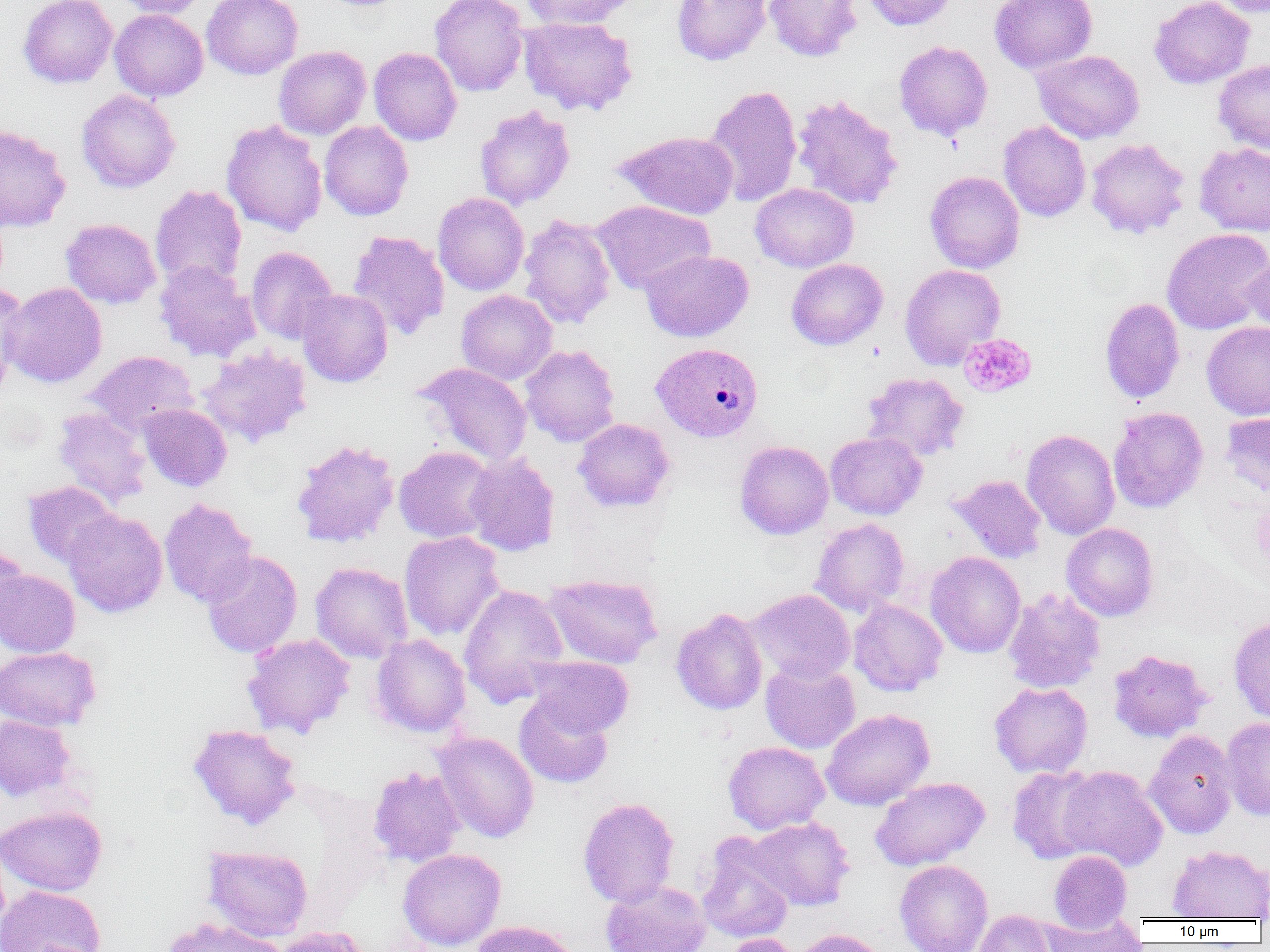

slide-level diagnosis = Plasmodium vivax
uninfected red blood cell locations = approximate bounding boxes as named x1/y1/x2/y2 corners in pixels: (x1=18, y1=0, x2=117, y2=88), (x1=113, y1=0, x2=209, y2=18), (x1=202, y1=0, x2=303, y2=79), (x1=429, y1=0, x2=529, y2=97), (x1=520, y1=0, x2=639, y2=29), (x1=671, y1=0, x2=771, y2=66), (x1=763, y1=0, x2=863, y2=61), (x1=862, y1=0, x2=957, y2=31), (x1=990, y1=0, x2=1098, y2=74), (x1=1149, y1=0, x2=1254, y2=89), (x1=1212, y1=0, x2=1270, y2=18), (x1=109, y1=9, x2=209, y2=101), (x1=518, y1=15, x2=638, y2=116), (x1=894, y1=40, x2=992, y2=141), (x1=273, y1=45, x2=371, y2=140), (x1=369, y1=47, x2=462, y2=146), (x1=1032, y1=49, x2=1144, y2=143), (x1=1213, y1=59, x2=1270, y2=154), (x1=704, y1=84, x2=802, y2=208), (x1=77, y1=89, x2=181, y2=193), (x1=791, y1=93, x2=903, y2=210), (x1=474, y1=105, x2=575, y2=210), (x1=221, y1=120, x2=327, y2=237), (x1=319, y1=121, x2=414, y2=220), (x1=998, y1=121, x2=1091, y2=222), (x1=0, y1=124, x2=71, y2=233), (x1=615, y1=130, x2=739, y2=219), (x1=1086, y1=138, x2=1190, y2=238), (x1=1194, y1=142, x2=1270, y2=236), (x1=924, y1=171, x2=1025, y2=273), (x1=750, y1=183, x2=859, y2=272), (x1=150, y1=184, x2=247, y2=292), (x1=432, y1=193, x2=529, y2=295), (x1=593, y1=200, x2=716, y2=294), (x1=518, y1=214, x2=617, y2=329), (x1=61, y1=218, x2=161, y2=309), (x1=1161, y1=227, x2=1270, y2=335), (x1=348, y1=230, x2=450, y2=342), (x1=246, y1=247, x2=338, y2=344), (x1=641, y1=249, x2=753, y2=342), (x1=1242, y1=252, x2=1270, y2=336), (x1=786, y1=258, x2=887, y2=350), (x1=154, y1=261, x2=260, y2=362), (x1=900, y1=264, x2=1006, y2=369), (x1=1, y1=282, x2=107, y2=388), (x1=0, y1=284, x2=28, y2=393), (x1=296, y1=289, x2=393, y2=387), (x1=456, y1=289, x2=557, y2=385), (x1=1099, y1=297, x2=1185, y2=404), (x1=1202, y1=322, x2=1270, y2=420), (x1=198, y1=344, x2=312, y2=448), (x1=520, y1=344, x2=620, y2=447), (x1=85, y1=350, x2=198, y2=437), (x1=414, y1=363, x2=533, y2=467), (x1=862, y1=372, x2=969, y2=461), (x1=138, y1=403, x2=232, y2=492), (x1=1108, y1=406, x2=1208, y2=513), (x1=53, y1=407, x2=152, y2=507), (x1=1220, y1=411, x2=1270, y2=498), (x1=573, y1=418, x2=675, y2=512), (x1=1022, y1=429, x2=1120, y2=540), (x1=826, y1=431, x2=927, y2=519), (x1=290, y1=438, x2=400, y2=549), (x1=735, y1=441, x2=833, y2=539), (x1=394, y1=446, x2=497, y2=543), (x1=463, y1=452, x2=560, y2=556), (x1=948, y1=474, x2=1047, y2=564), (x1=22, y1=481, x2=121, y2=568), (x1=159, y1=498, x2=257, y2=607), (x1=63, y1=510, x2=167, y2=617), (x1=811, y1=518, x2=910, y2=617), (x1=1061, y1=523, x2=1159, y2=621), (x1=399, y1=531, x2=504, y2=640), (x1=0, y1=544, x2=29, y2=635), (x1=202, y1=551, x2=303, y2=658), (x1=925, y1=551, x2=1026, y2=657), (x1=310, y1=562, x2=413, y2=664), (x1=0, y1=570, x2=80, y2=657), (x1=543, y1=574, x2=662, y2=668), (x1=458, y1=584, x2=568, y2=707), (x1=1003, y1=587, x2=1106, y2=694), (x1=747, y1=588, x2=855, y2=684), (x1=849, y1=599, x2=947, y2=696), (x1=671, y1=608, x2=768, y2=715), (x1=1228, y1=616, x2=1270, y2=725), (x1=242, y1=633, x2=355, y2=739), (x1=370, y1=634, x2=471, y2=738), (x1=0, y1=646, x2=101, y2=730), (x1=1108, y1=649, x2=1211, y2=743), (x1=526, y1=656, x2=634, y2=737), (x1=760, y1=661, x2=860, y2=754), (x1=989, y1=682, x2=1093, y2=777), (x1=514, y1=694, x2=614, y2=789), (x1=821, y1=709, x2=934, y2=810), (x1=0, y1=714, x2=76, y2=801), (x1=1221, y1=716, x2=1270, y2=820), (x1=189, y1=724, x2=301, y2=830), (x1=1145, y1=729, x2=1238, y2=838), (x1=432, y1=731, x2=539, y2=843), (x1=723, y1=741, x2=830, y2=834), (x1=1005, y1=765, x2=1103, y2=864), (x1=1058, y1=765, x2=1168, y2=871), (x1=368, y1=766, x2=466, y2=868), (x1=870, y1=777, x2=990, y2=871), (x1=578, y1=796, x2=680, y2=908), (x1=0, y1=806, x2=107, y2=895), (x1=746, y1=816, x2=855, y2=911), (x1=697, y1=838, x2=794, y2=944), (x1=203, y1=845, x2=313, y2=941), (x1=1167, y1=845, x2=1270, y2=920), (x1=397, y1=848, x2=506, y2=951), (x1=1049, y1=850, x2=1132, y2=932), (x1=894, y1=859, x2=993, y2=952), (x1=600, y1=879, x2=711, y2=952), (x1=0, y1=885, x2=106, y2=952), (x1=971, y1=909, x2=1059, y2=952), (x1=160, y1=917, x2=286, y2=952), (x1=1040, y1=917, x2=1144, y2=951), (x1=470, y1=920, x2=580, y2=952), (x1=274, y1=926, x2=369, y2=952), (x1=791, y1=928, x2=888, y2=952), (x1=720, y1=934, x2=802, y2=952)
modality = optical microscopy
preparation = thin blood smear
Plasmodium vivax-infected red blood cell locations = approximate bounding boxes as named x1/y1/x2/y2 corners in pixels: (x1=651, y1=342, x2=764, y2=442)
image size = 1270×952 pixels
magnification = 1000x
platelet locations = approximate bounding boxes as named x1/y1/x2/y2 corners in pixels: (x1=958, y1=332, x2=1037, y2=398)
field of view = one of a larger specimen